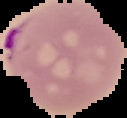
image type = segmented cell region on a black background
preparation = thin blood film
image size = 127×118 pixels
malaria status = parasitized